Comment on the morphology of the erythrocytes.
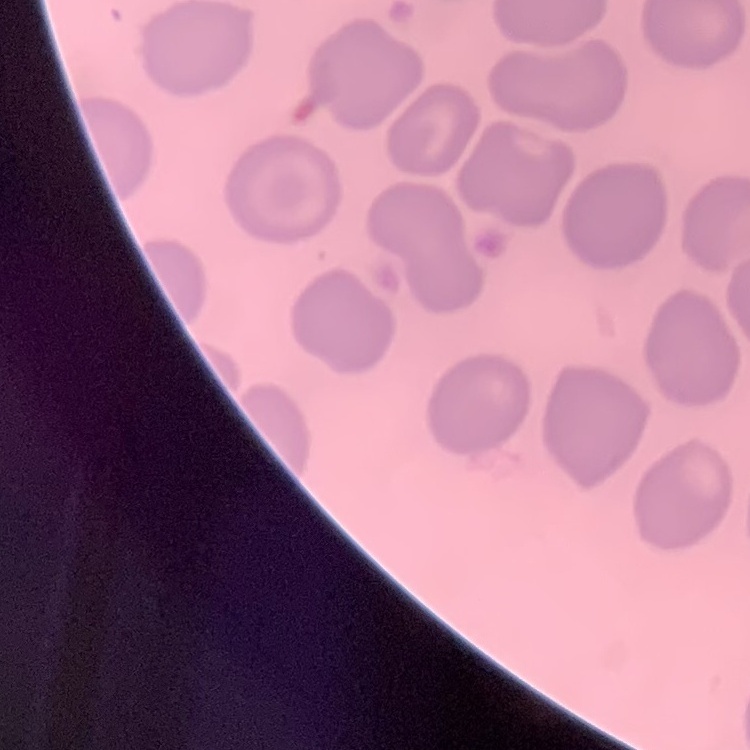

They show no rouleaux formation.

Summary:
  - Image type: one tile cut from a larger photomicrograph
  - Preparation: thin peripheral smear
  - Stain: Field's or Giemsa